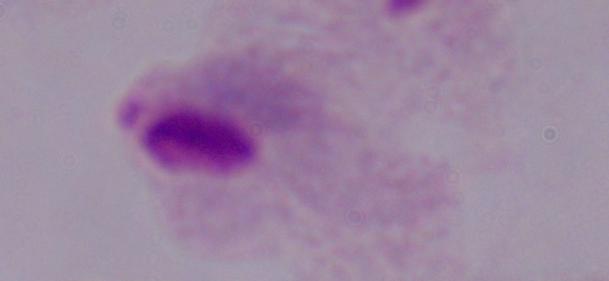

magnification = 1000x
identification = trichomonad
modality = photomicrograph